Report the malaria status of this cell.
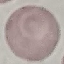

Uninfected.

Acquired by smartphone through the microscope eyepiece. Thin blood smear. Giemsa-stained preparation. Cell patch, automatically extracted from a larger field of view and resized to 64 × 64 pixels.